Point out every Plasmodium parasite and every leukocyte.
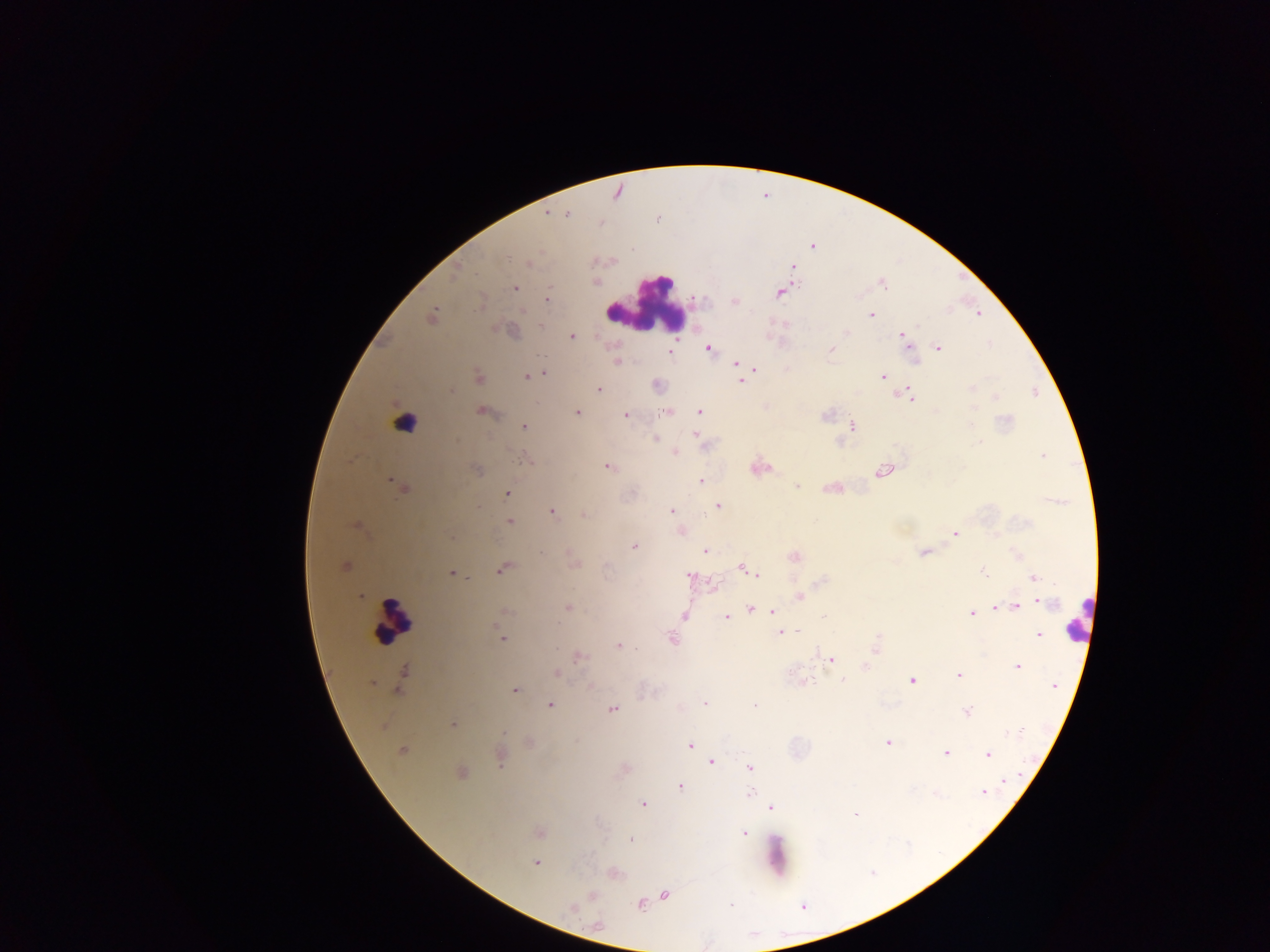

Approximate centers as x y in pixels.
Plasmodium parasites: 546 213; 568 213; 657 217; 812 245; 527 263; 792 268; 455 271; 596 280; 882 283; 514 288; 781 291; 546 298; 734 301; 870 313; 978 313; 432 315; 901 335; 572 336; 938 347; 708 348; 830 349; 670 353; 616 361; 735 362; 754 369; 543 372; 534 374; 526 375; 883 376; 477 378; 740 380; 656 386; 971 388; 598 389; 449 390; 911 397; 995 397; 667 410; 481 411; 699 411; 576 412; 626 415; 524 426; 852 426; 695 434; 655 438; 675 452; 1043 455; 607 466; 759 467; 476 469; 882 470; 699 481; 400 485; 797 486; 833 487; 506 494; 717 506; 671 510; 551 511; 584 515; 509 521; 357 526; 680 531; 954 534; 634 547; 704 550; 924 552; 794 557; 343 565; 741 567; 502 569; 984 572; 452 573; 757 575; 688 576; 1033 577; 713 584; 361 595; 798 596; 1038 600; 1015 606; 567 607; 750 608; 994 608; 504 612; 773 612; 971 613; 684 615; 725 617; 781 632; 1038 634; 671 638; 502 639; 618 645; 875 648; 578 656; 831 660; 864 666; 1018 666; 557 673; 958 675; 402 678; 843 678; 911 680; 803 682; 1053 685; 590 687; 514 691; 705 702; 550 704; 754 706; 612 709; 966 710; 453 724; 528 742; 888 742; 691 745; 401 750; 947 752; 987 755; 499 757; 711 760; 750 767; 460 772; 1004 780; 679 786; 983 791; 750 794; 642 803; 769 807; 854 814; 538 833; 743 833; 629 839; 535 863; 613 873; 663 894; 591 895; 639 904; 571 907; 597 925.
Leukocytes: 648 302; 404 422; 1081 620; 391 622; 775 855.

Summary:
  - Capture: mobile-phone photograph through a microscope
  - Preparation: thick blood film
  - Country: Ghana
  - Image size: 1270×952 pixels
  - Field of view: single